Classify this cell by malaria status.
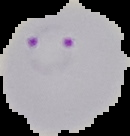

It is parasitized.

Image is 130×136 pixels. From a thin blood film. The area outside the segmented cell region is set to black.